Outline platelets.
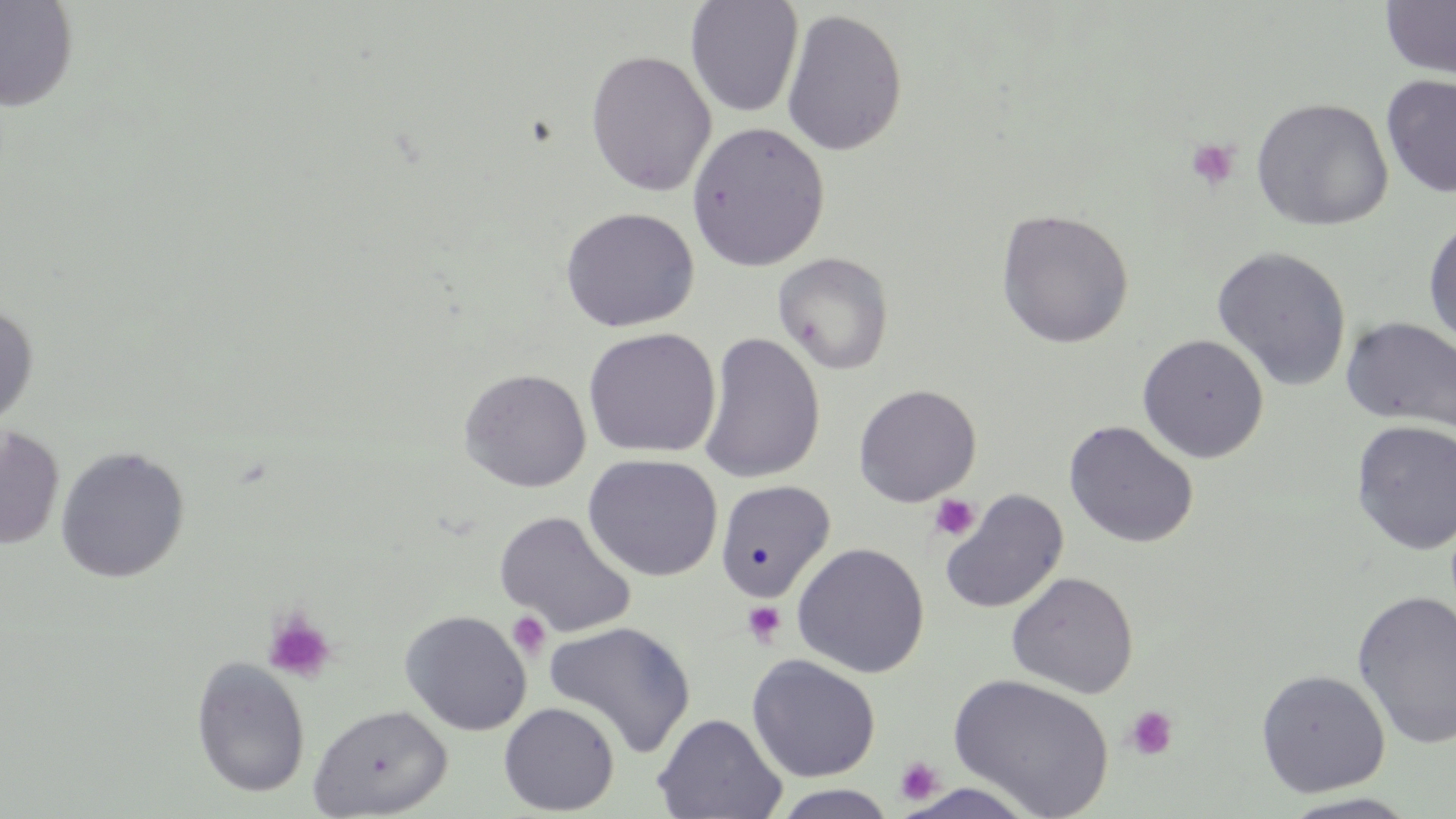

Approximate bounding boxes as named x1/y1/x2/y2 corners in pixels.
Platelets: (x1=1184, y1=137, x2=1241, y2=192), (x1=928, y1=493, x2=982, y2=542), (x1=742, y1=601, x2=787, y2=647), (x1=262, y1=610, x2=337, y2=684), (x1=507, y1=611, x2=551, y2=659), (x1=1126, y1=706, x2=1178, y2=760), (x1=894, y1=755, x2=945, y2=806).

Uninfected red blood cell locations: (x1=0, y1=0, x2=80, y2=112), (x1=685, y1=0, x2=804, y2=118), (x1=1381, y1=1, x2=1456, y2=79), (x1=781, y1=8, x2=908, y2=157), (x1=585, y1=50, x2=718, y2=196), (x1=1381, y1=74, x2=1456, y2=198), (x1=1251, y1=97, x2=1394, y2=232), (x1=687, y1=121, x2=830, y2=272), (x1=560, y1=206, x2=700, y2=333), (x1=996, y1=208, x2=1134, y2=348), (x1=1423, y1=216, x2=1456, y2=353), (x1=1211, y1=245, x2=1352, y2=391), (x1=773, y1=252, x2=894, y2=375), (x1=0, y1=303, x2=38, y2=430), (x1=1341, y1=316, x2=1456, y2=433), (x1=582, y1=327, x2=721, y2=459), (x1=699, y1=332, x2=825, y2=484), (x1=1137, y1=334, x2=1269, y2=463), (x1=458, y1=368, x2=592, y2=492), (x1=853, y1=384, x2=981, y2=507), (x1=1350, y1=419, x2=1456, y2=556), (x1=1063, y1=420, x2=1199, y2=549), (x1=0, y1=425, x2=65, y2=551), (x1=55, y1=445, x2=190, y2=583), (x1=582, y1=454, x2=723, y2=582), (x1=714, y1=479, x2=835, y2=602), (x1=939, y1=490, x2=1069, y2=615), (x1=495, y1=510, x2=637, y2=638), (x1=792, y1=542, x2=930, y2=679), (x1=1006, y1=571, x2=1139, y2=699), (x1=1352, y1=589, x2=1456, y2=750), (x1=400, y1=610, x2=532, y2=736), (x1=543, y1=621, x2=696, y2=759), (x1=746, y1=654, x2=881, y2=783), (x1=190, y1=658, x2=311, y2=798), (x1=1256, y1=668, x2=1390, y2=797), (x1=947, y1=673, x2=1115, y2=819), (x1=499, y1=702, x2=620, y2=815), (x1=307, y1=704, x2=452, y2=818), (x1=653, y1=713, x2=786, y2=819), (x1=771, y1=785, x2=899, y2=819), (x1=1277, y1=793, x2=1424, y2=818). Slide-level diagnosis: no evidence of blood parasites. Image is 1456×819 pixels. 1000x magnification. Thin blood smear. One field of a larger specimen. May-Grünwald-Giemsa-stained preparation. Optical microscopy.